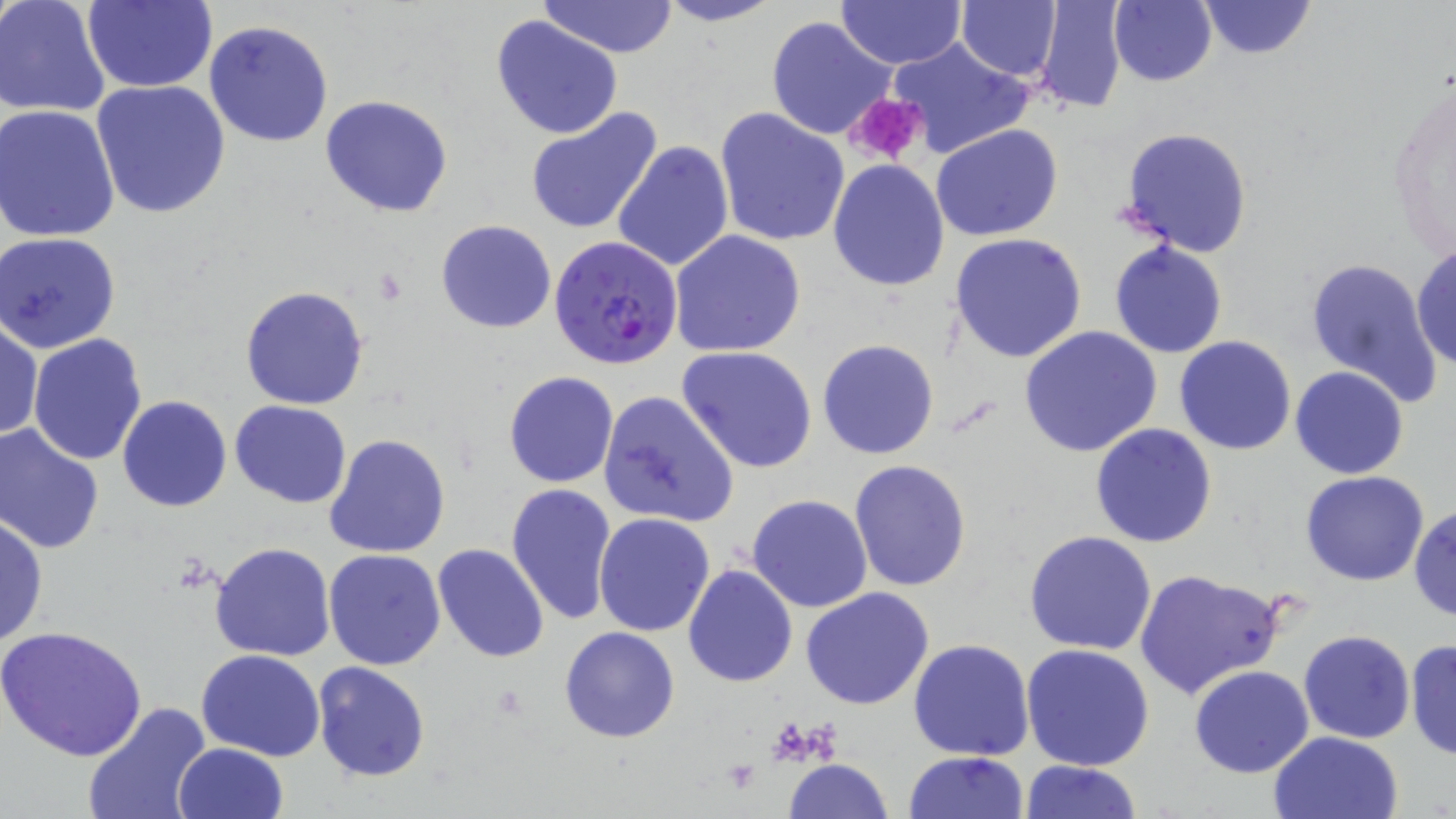

Summary:
  - Coordinate format: approximate bounding boxes as (x1,y1)-(x2,y2) corner pairs in pixels
  - Platelet locations: (844,92)-(929,166)
  - Plasmodium falciparum-infected red blood cell locations: (549,235)-(683,372)
  - Uninfected red blood cell locations: (0,0)-(110,119), (81,0)-(217,92), (537,0)-(680,57), (655,0)-(786,27), (833,0)-(967,70), (957,0)-(1062,81), (1031,0)-(1127,116), (1109,0)-(1216,86), (1199,0)-(1316,59), (491,15)-(623,140), (766,17)-(897,141), (204,19)-(333,147), (887,36)-(1031,160), (1386,70)-(1455,268), (91,79)-(231,220), (320,95)-(453,219), (0,105)-(121,243), (715,108)-(850,248), (525,109)-(662,235), (932,123)-(1061,241), (1118,126)-(1254,257), (613,141)-(733,273), (827,160)-(949,291), (435,219)-(557,334), (670,229)-(805,357), (1,232)-(122,353), (949,232)-(1088,363), (1108,239)-(1228,360), (1411,242)-(1456,370), (1303,257)-(1443,404), (241,285)-(369,410), (1,316)-(42,443), (1018,327)-(1163,458), (27,333)-(147,466), (1173,336)-(1297,455), (817,339)-(939,459), (677,346)-(817,473), (1289,366)-(1410,480), (502,371)-(620,488), (598,390)-(739,528), (117,395)-(231,512), (230,400)-(352,507), (1090,423)-(1217,549), (0,424)-(105,555), (324,433)-(450,558), (849,459)-(972,593), (1301,471)-(1430,586), (506,484)-(617,626), (747,494)-(873,611), (1410,504)-(1455,621), (594,514)-(714,636), (0,515)-(47,649), (1023,530)-(1158,655), (209,541)-(337,662), (431,543)-(551,664), (323,548)-(446,671), (682,564)-(798,686), (1133,568)-(1287,702), (801,588)-(935,710), (1,626)-(147,762), (559,626)-(680,744), (1298,631)-(1416,744), (1405,637)-(1455,760), (908,638)-(1034,760), (1020,644)-(1155,771), (197,649)-(326,763), (312,663)-(431,783), (1189,665)-(1315,777), (82,702)-(211,819), (1267,730)-(1403,819), (172,743)-(288,819), (904,751)-(1029,819), (784,758)-(893,819), (1019,759)-(1142,818)
  - Slide-level diagnosis: Plasmodium falciparum
  - Modality: light microscopy
  - Stain: May-Grünwald-Giemsa
  - Magnification: 1000x
  - Image size: 1456×819 pixels
  - Preparation: thin blood smear
  - Field of view: one of a larger specimen